Identify the parasite.
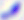
Toxoplasma gondii.

Summary:
  - Magnification: 400x
  - Modality: photomicrograph